Locate the cells, classifying each as a parasitized RBC, an uninfected RBC, or a WBC.
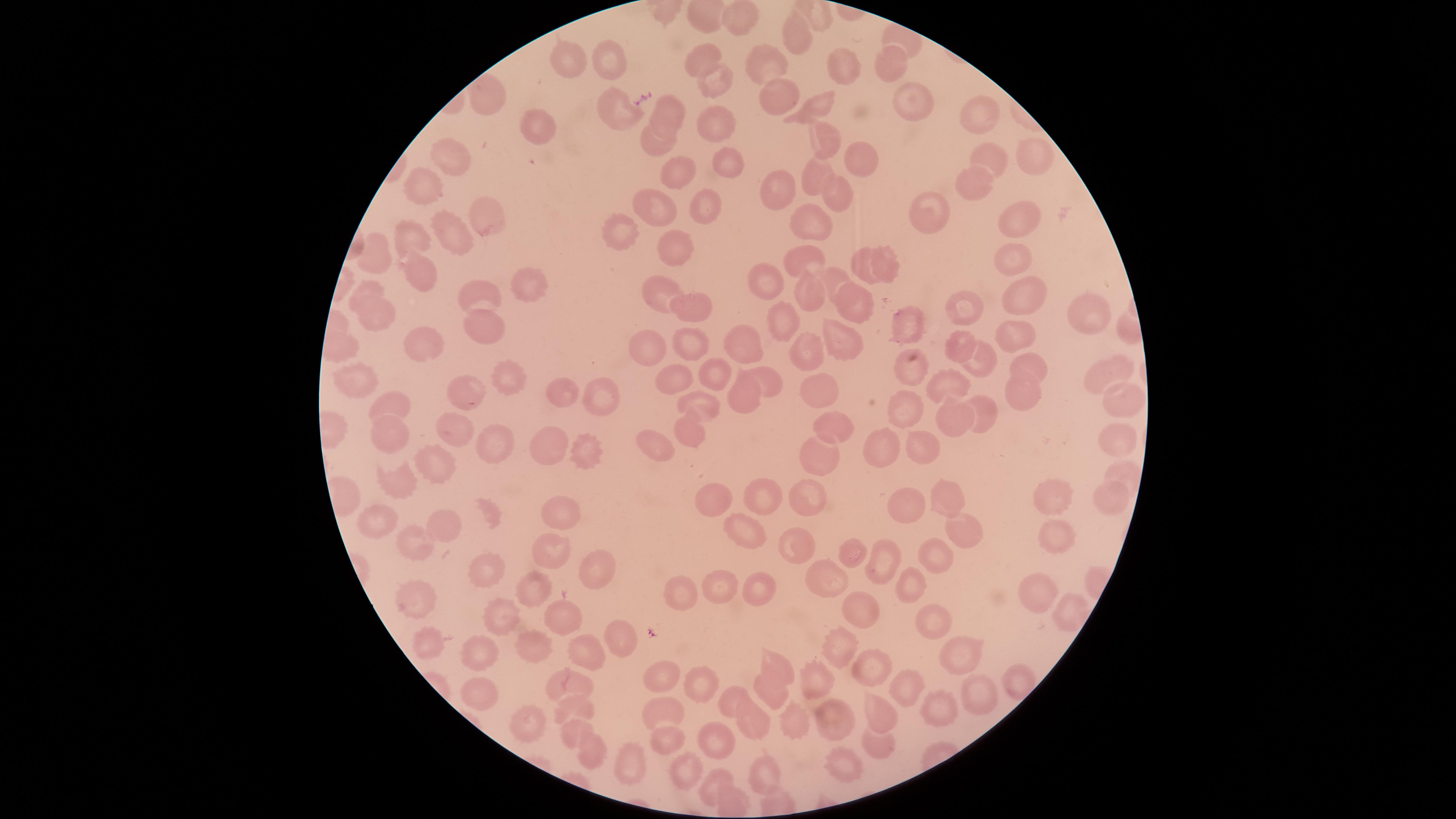

No parasitized RBCs identified.
Approximate marker points as (x, y) in pixels.
Uninfected RBCs: (736, 19), (796, 38), (703, 58), (570, 60), (608, 61), (891, 63), (769, 65), (840, 67), (716, 87), (776, 95), (609, 102), (905, 108), (676, 109), (816, 109), (983, 113), (713, 123), (540, 128), (662, 128), (820, 132), (656, 148), (862, 157), (993, 159), (1037, 160), (455, 163), (727, 163), (677, 174), (819, 174), (968, 177), (779, 188), (428, 192), (836, 192), (655, 203), (705, 204), (483, 209), (924, 211), (808, 218), (1014, 222), (455, 234), (619, 236), (415, 239), (680, 249), (1007, 250), (377, 255), (882, 256), (807, 257), (863, 267), (420, 276), (831, 276), (768, 279), (512, 283), (661, 285), (367, 289), (810, 291), (1026, 296), (479, 299), (858, 304), (969, 305), (690, 307), (379, 313), (1091, 316), (781, 319), (915, 321), (489, 331), (1015, 333), (845, 339), (742, 342), (959, 342), (423, 343), (691, 343), (808, 348), (645, 351), (979, 359), (1039, 362), (718, 370), (908, 370), (1100, 371), (769, 373), (358, 374), (674, 379), (951, 379), (814, 384), (511, 386), (470, 387), (741, 388), (601, 391), (1022, 393), (1119, 396), (562, 398), (704, 399), (396, 401), (904, 406), (985, 412), (950, 419), (840, 421), (459, 429), (1110, 434), (692, 435), (391, 437), (649, 443), (552, 444), (487, 446), (917, 447), (884, 448), (588, 450), (818, 461), (436, 466), (1119, 475), (398, 485), (1061, 490), (948, 493), (764, 497), (807, 497), (714, 498), (1107, 498), (910, 503), (490, 512), (564, 512), (381, 517), (447, 521), (962, 526), (742, 532), (1053, 534), (556, 543), (421, 546), (799, 546), (937, 557), (849, 558), (484, 562), (888, 563), (597, 570), (827, 581), (538, 585), (720, 588), (754, 588), (680, 589), (915, 590), (1033, 590), (424, 601), (853, 603), (1073, 608), (931, 616), (506, 620), (564, 620), (616, 636), (429, 641), (844, 645), (540, 646), (959, 655), (590, 658), (476, 661), (774, 664), (881, 664), (668, 674), (702, 678), (1020, 681), (571, 683), (818, 683), (481, 688), (769, 690), (905, 691), (977, 693), (734, 695), (577, 707), (666, 711), (879, 712), (938, 713), (832, 721), (528, 723), (795, 723), (763, 726), (573, 729), (666, 737), (722, 740), (878, 747), (592, 751), (626, 761), (774, 768), (686, 770), (841, 772), (710, 789).
No WBCs identified.

Thin blood film. One field of view of the specimen. Image is 1456×819 pixels. Smartphone photograph through the microscope eyepiece. The visible region is circular. Giemsa-stained preparation.